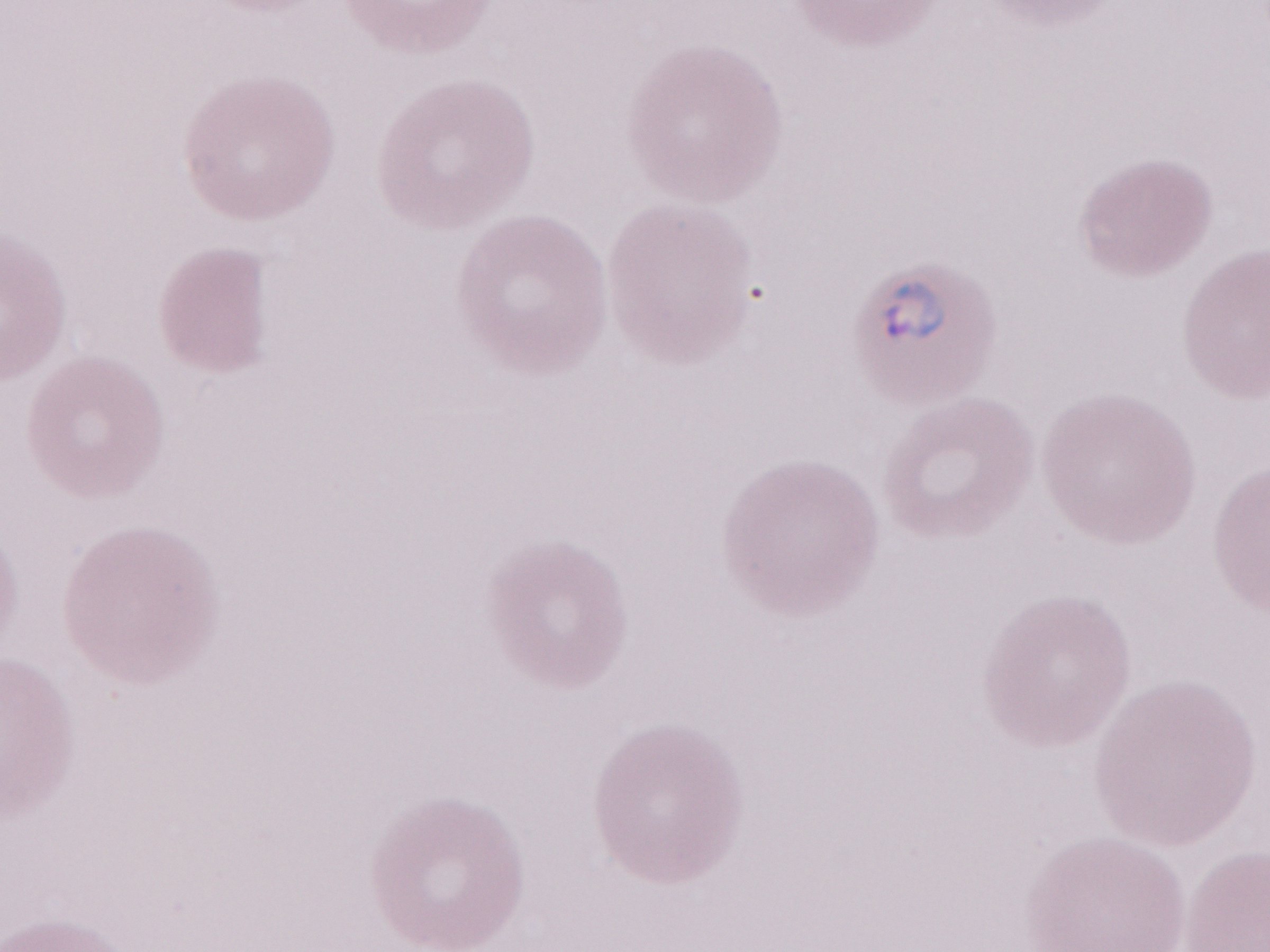

Patient-level malaria diagnosis: positive. Single field of view. 1,000x magnification. May-Grünwald-Giemsa stain. Image is 1270×952 pixels. Thin blood film. Olympus BX43 microscope, Olympus DP73 camera.